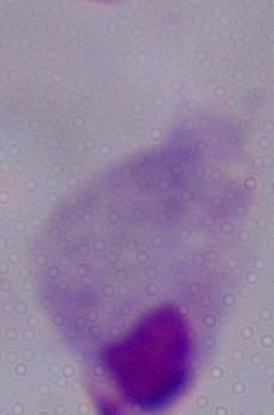 Captured at 1000x magnification. Photomicrograph. A trichomonad is seen.